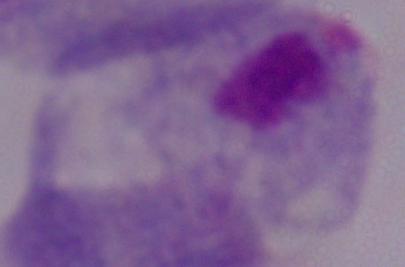

identification = trichomonad
modality = photomicrograph
magnification = 1000x